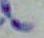 Toxoplasma gondii is shown. Photomicrograph. 1000x magnification.